Report the malaria status of this cell.
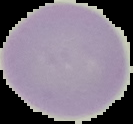

Uninfected.

Summary:
  - Preparation: thin blood smear
  - Image size: 133×124 pixels
  - Image type: cell region segmented out of the field of view; surrounding area masked to black